Report the malaria status of this cell.
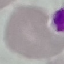
Uninfected.

Photographed with a smartphone camera at the microscope eyepiece. Thin blood film. Cell patch, automatically extracted from a larger field of view and resized to 64 × 64 pixels. Giemsa stain.